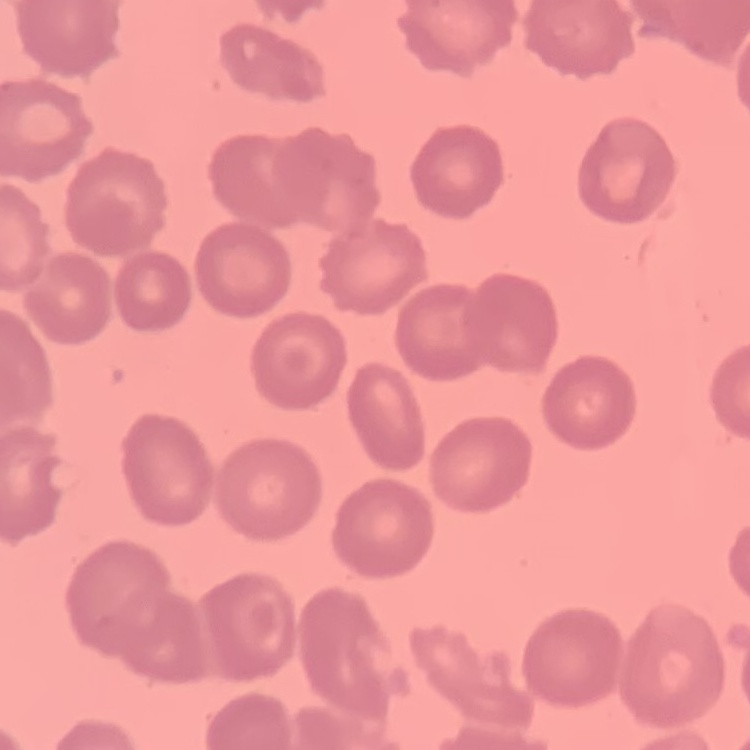
Summary:
  - Erythrocyte morphology: no rouleaux formation
  - Preparation: thin peripheral smear
  - Image type: one tile cut from a larger photomicrograph
  - Stain: Field's or Giemsa